Assess for parasitized red blood cells.
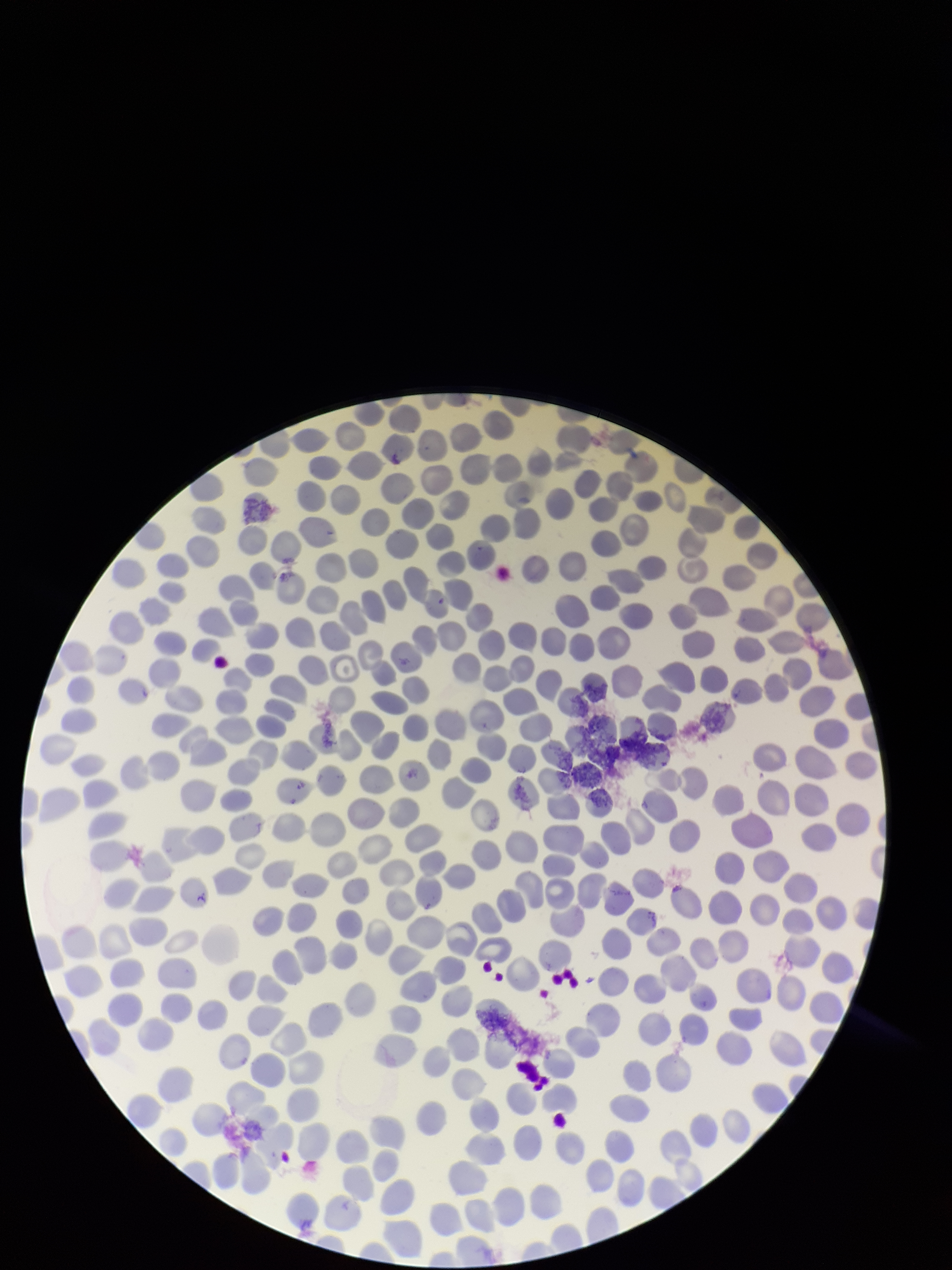
None identified.

preparation = thin
red blood cell count = 301
patient malaria status = negative
stain = Giemsa
capture = smartphone photograph through the microscope eyepiece
field of view = single
parasitized red blood cell count = 0
image size = 952×1270 pixels